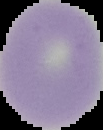

Summary:
  - Image size: 103×130 pixels
  - Image type: segmented cell region with the area outside set to black
  - Preparation: thin blood smear
  - Malaria status: uninfected